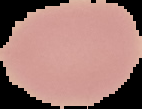
image size = 142×109 pixels
malaria status = uninfected
image type = segmented cell region on a black background
preparation = thin blood film